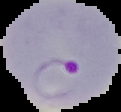 From a thin blood smear. Malaria status: parasitized. Cell region segmented out of the field of view; the surrounding area is masked to black. Image is 121×112 pixels.